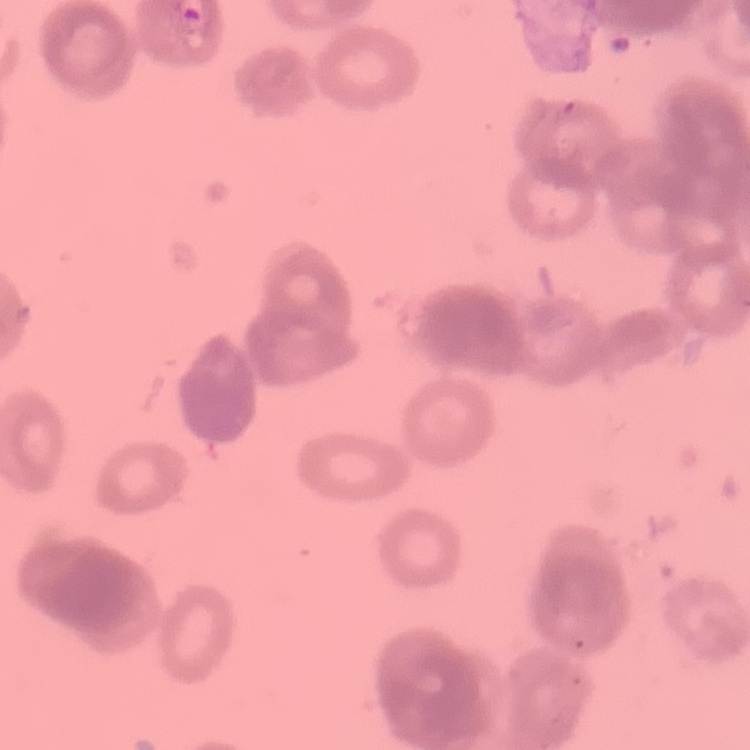

The erythrocytes show rouleaux formation. Field's or Giemsa stain. Square crop of a larger photomicrograph. Thin blood smear.